Classify this cell by malaria status.
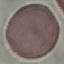

Uninfected.

Summary:
  - Preparation: thin blood film
  - Stain: Giemsa
  - Image type: cell patch, automatically extracted from a larger field of view and resized to 64 × 64 pixels
  - Capture: smartphone through the microscope eyepiece